Assess this cell for malaria.
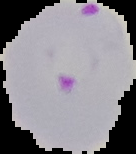
Parasitized.

{
  "image_size": "136×154 pixels",
  "preparation": "thin blood smear",
  "image_type": "segmented cell region on a black background"
}